Give the position of every Plasmodium parasite.
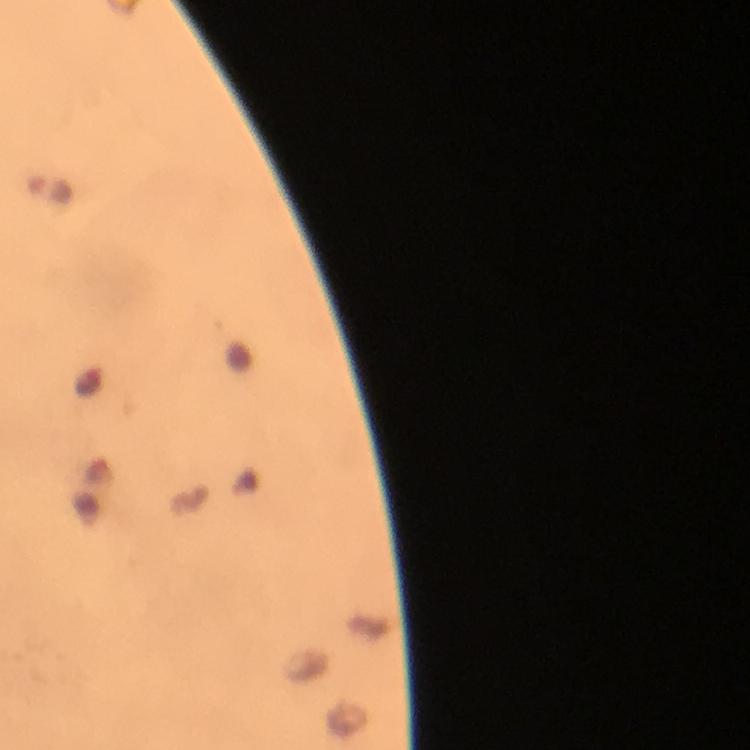

Approximate centers as [x, y] in pixels.
Plasmodium parasites: [49, 187].

stain = Giemsa
preparation = thick blood film
capture = smartphone photograph through a microscope
immersion oil = applied
magnification = 100x
context = from a malaria diagnostic workup
cropped from = one field of view
image size = 750×750 pixels